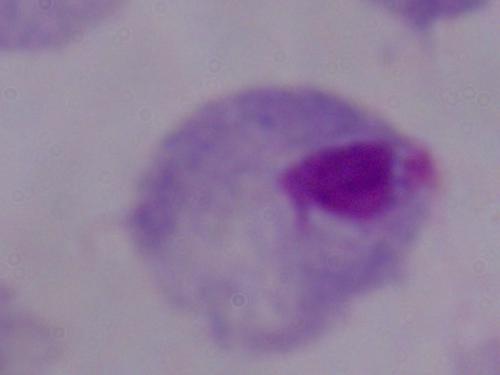

Captured at 1000x magnification. A trichomonad is shown. Micrograph.